State which parasite is depicted.
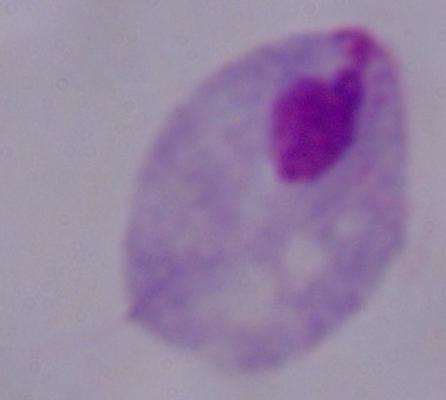
This is a trichomonad.

magnification = 1000x
modality = photomicrograph